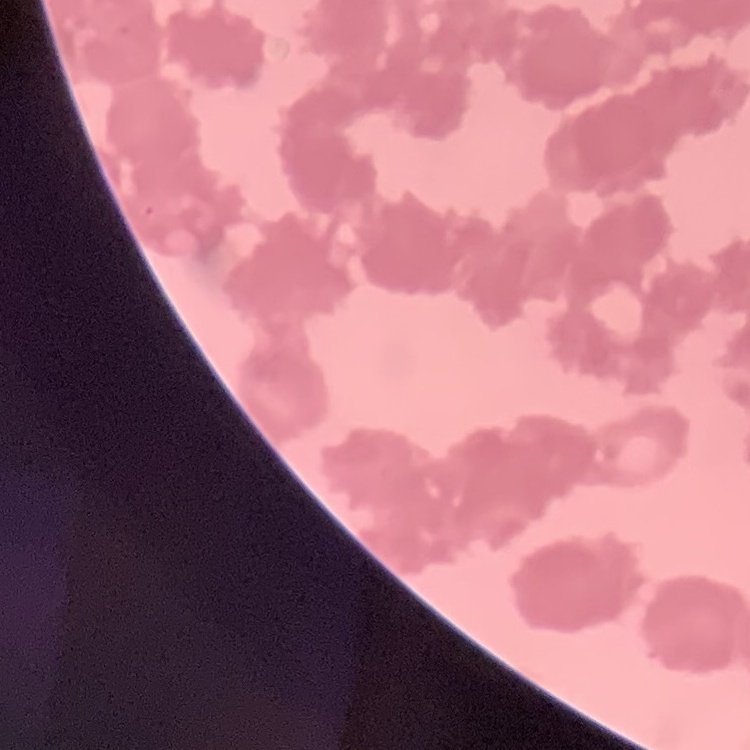
The red blood cells show rouleaux formation. Square crop of a larger photomicrograph. Thin peripheral smear. Field's or Giemsa stain.